State which parasite is depicted.
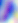
This is Toxoplasma gondii.

Photomicrograph. 400x magnification.